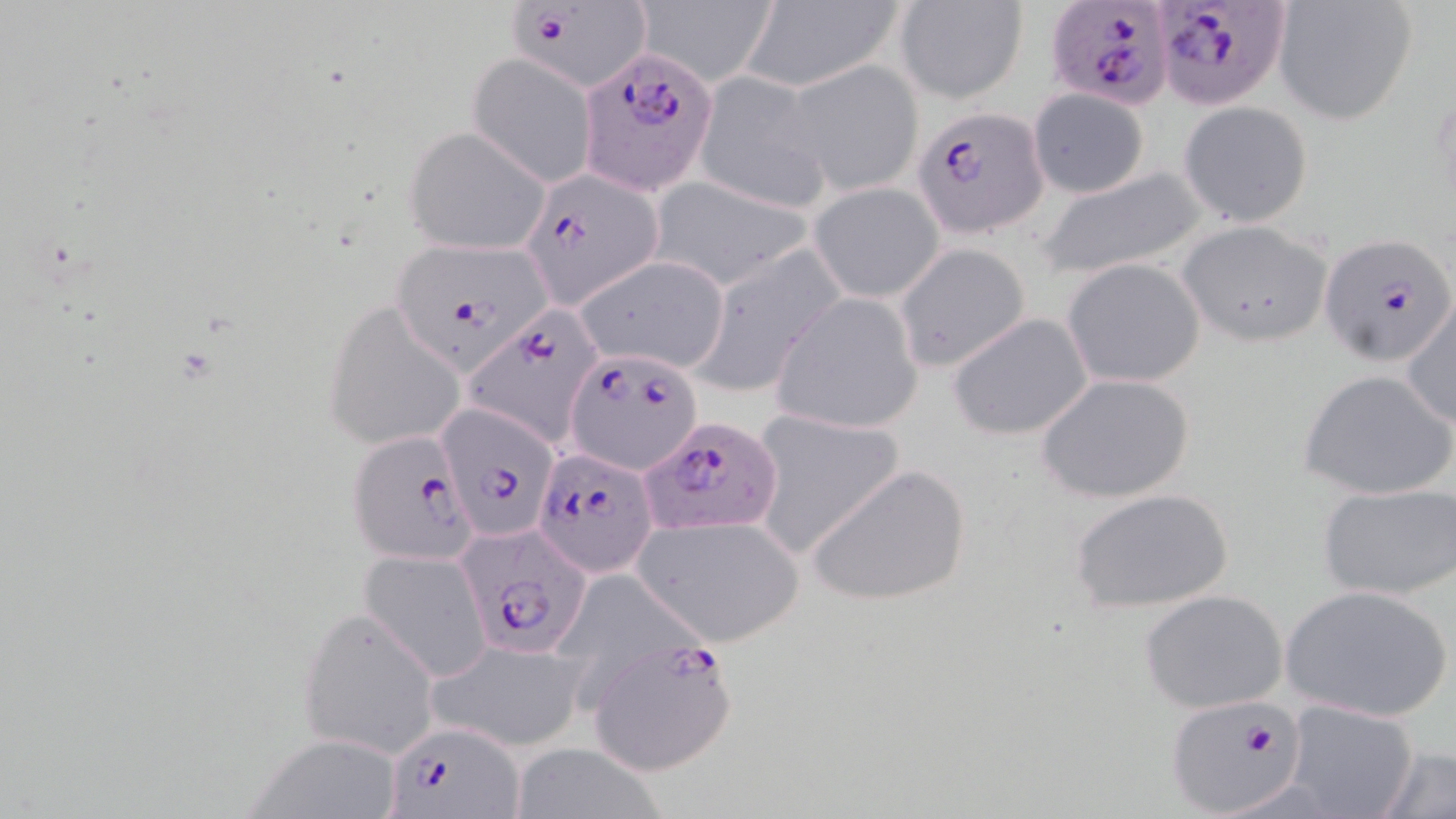
Approximate bounding boxes as named x1/y1/x2/y2 corners in pixels. Plasmodium falciparum-infected red blood cell locations: (x1=507, y1=0, x2=645, y2=84), (x1=1154, y1=1, x2=1292, y2=109), (x1=1046, y1=3, x2=1172, y2=111), (x1=582, y1=48, x2=721, y2=196), (x1=915, y1=106, x2=1047, y2=238), (x1=519, y1=165, x2=662, y2=305), (x1=1322, y1=234, x2=1454, y2=366), (x1=389, y1=238, x2=555, y2=375), (x1=460, y1=307, x2=606, y2=447), (x1=563, y1=346, x2=700, y2=492), (x1=437, y1=401, x2=562, y2=545), (x1=644, y1=415, x2=783, y2=538), (x1=345, y1=430, x2=481, y2=567), (x1=533, y1=447, x2=658, y2=577), (x1=455, y1=523, x2=595, y2=659), (x1=585, y1=634, x2=739, y2=777), (x1=1164, y1=696, x2=1305, y2=816), (x1=386, y1=718, x2=525, y2=819). Uninfected red blood cell locations: (x1=1273, y1=0, x2=1418, y2=126), (x1=636, y1=1, x2=779, y2=88), (x1=741, y1=1, x2=904, y2=92), (x1=894, y1=1, x2=1029, y2=104), (x1=466, y1=55, x2=598, y2=188), (x1=783, y1=59, x2=924, y2=197), (x1=693, y1=69, x2=831, y2=213), (x1=1027, y1=89, x2=1150, y2=199), (x1=1178, y1=101, x2=1314, y2=228), (x1=403, y1=125, x2=552, y2=255), (x1=1037, y1=165, x2=1210, y2=282), (x1=647, y1=174, x2=814, y2=292), (x1=808, y1=181, x2=945, y2=303), (x1=1179, y1=219, x2=1332, y2=348), (x1=894, y1=242, x2=1032, y2=372), (x1=693, y1=244, x2=846, y2=395), (x1=572, y1=254, x2=732, y2=375), (x1=1063, y1=258, x2=1206, y2=388), (x1=768, y1=293, x2=924, y2=433), (x1=326, y1=301, x2=467, y2=451), (x1=1402, y1=301, x2=1455, y2=429), (x1=947, y1=313, x2=1093, y2=441), (x1=1298, y1=368, x2=1456, y2=501), (x1=1036, y1=372, x2=1196, y2=505), (x1=747, y1=408, x2=908, y2=560), (x1=806, y1=463, x2=972, y2=607), (x1=1318, y1=482, x2=1455, y2=601), (x1=1072, y1=487, x2=1234, y2=615), (x1=631, y1=514, x2=806, y2=647), (x1=358, y1=548, x2=493, y2=680), (x1=1281, y1=584, x2=1452, y2=724), (x1=1139, y1=589, x2=1288, y2=713), (x1=297, y1=607, x2=441, y2=758), (x1=424, y1=638, x2=586, y2=752), (x1=1284, y1=699, x2=1419, y2=819), (x1=248, y1=736, x2=402, y2=818), (x1=504, y1=742, x2=672, y2=819), (x1=1374, y1=746, x2=1456, y2=819). Slide-level diagnosis: Plasmodium falciparum. Light microscopy. One field of a larger specimen. Thin blood smear. Image is 1456×819 pixels. May-Grünwald-Giemsa stain. Captured at 1000x magnification.